Classify this cell by malaria status.
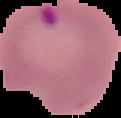
Parasitized.

From a thin blood film. Image is 121×118 pixels. The area outside the segmented cell region is set to black.